Locate and identify every blood parasite.
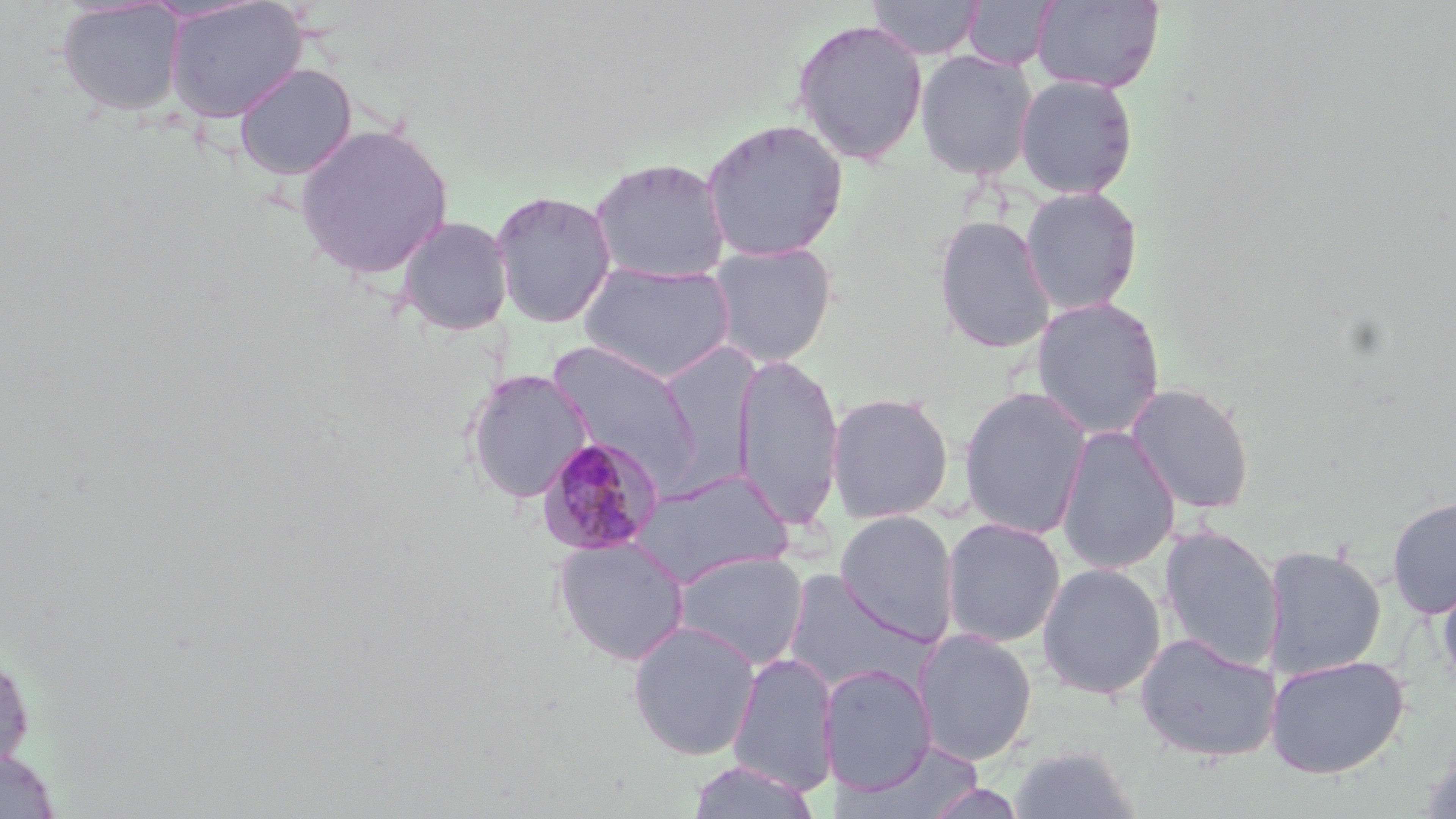

Approximate bounding boxes as [x1, y1, x2, y2] in pixels.
Plasmodium malariae-infected red blood cells: [535, 435, 664, 557].
No Plasmodium falciparum, Plasmodium ovale, Plasmodium vivax, Babesia divergens, or Trypanosoma brucei observed.

Uninfected red blood cell locations: [163, 0, 308, 123], [867, 0, 982, 59], [1031, 0, 1164, 92], [54, 1, 188, 117], [963, 1, 1057, 71], [790, 17, 929, 166], [915, 49, 1038, 180], [234, 63, 357, 180], [1014, 74, 1139, 199], [700, 117, 849, 262], [293, 121, 455, 281], [589, 157, 732, 285], [1019, 186, 1144, 315], [489, 189, 618, 329], [395, 215, 513, 336], [933, 215, 1056, 354], [706, 242, 837, 368], [577, 260, 736, 384], [1030, 297, 1166, 440], [733, 352, 845, 532], [463, 370, 592, 503], [1124, 382, 1256, 515], [958, 385, 1093, 540], [826, 391, 955, 524], [1056, 425, 1180, 575], [629, 469, 793, 588], [1386, 495, 1456, 619], [835, 510, 959, 646], [941, 517, 1066, 648], [1158, 523, 1284, 673], [552, 535, 690, 666], [1262, 543, 1387, 679], [673, 550, 809, 670], [1037, 563, 1166, 700], [1436, 566, 1456, 704], [782, 569, 932, 696], [627, 620, 761, 760], [913, 628, 1038, 765], [1134, 632, 1281, 763], [1, 649, 34, 772], [727, 652, 838, 796], [1265, 654, 1410, 778], [820, 663, 936, 794], [843, 737, 986, 819], [1421, 739, 1456, 819], [1008, 744, 1140, 819], [0, 747, 60, 818], [687, 759, 819, 818], [920, 779, 1030, 819]. Slide-level diagnosis: Plasmodium malariae. 1000x magnification. Image is 1456×819 pixels. Light microscopy. Thin blood smear. Single field of view. May-Grünwald-Giemsa-stained preparation.